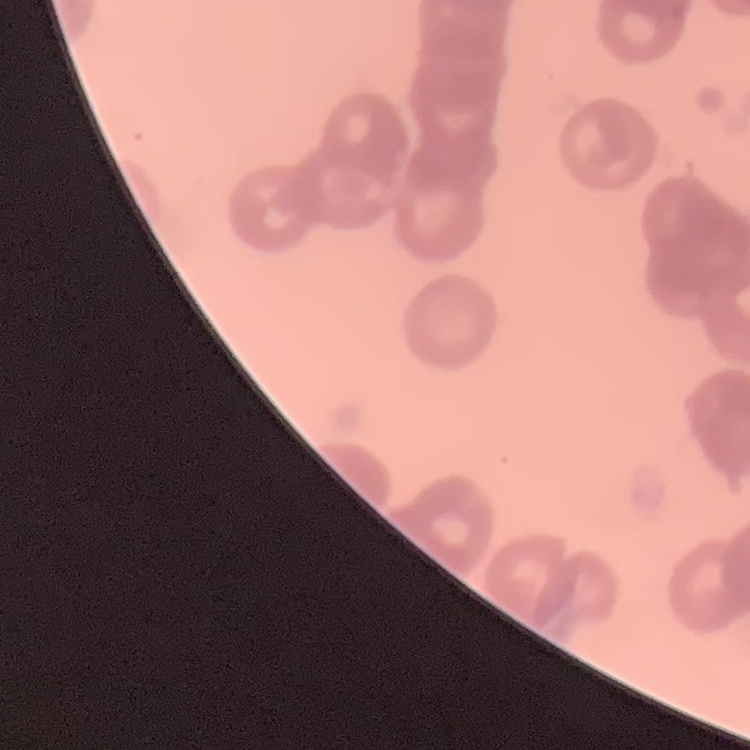 The red blood cells show rouleaux formation. Square crop of a larger photomicrograph. Thin blood smear. Stained with either Field's or Giemsa.